Outline each Plasmodium falciparum-infected red blood cell.
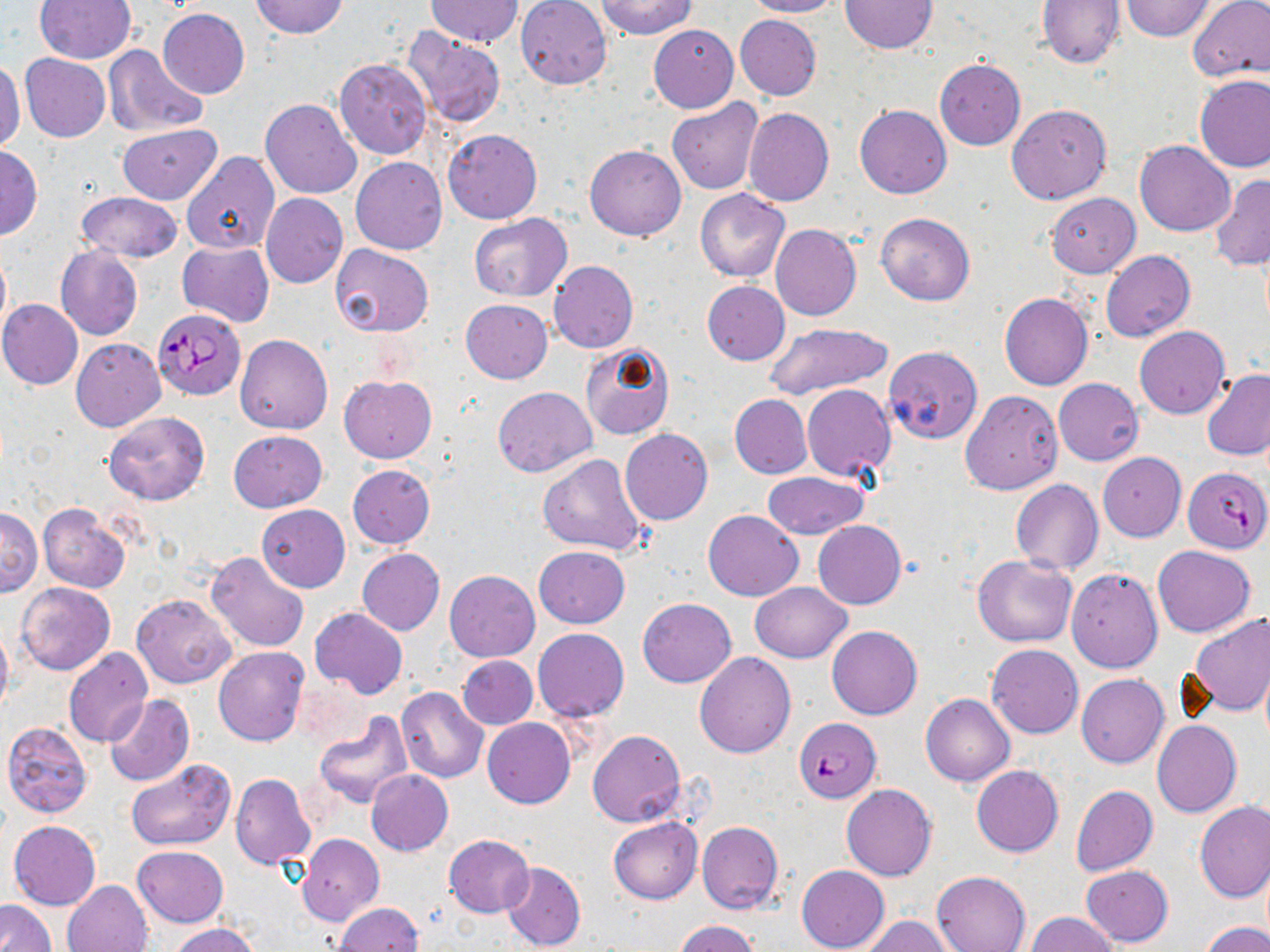

Approximate bounding boxes as named x1/y1/x2/y2 corners in pixels.
Plasmodium falciparum-infected red blood cells: (x1=152, y1=310, x2=245, y2=400), (x1=1184, y1=467, x2=1269, y2=553), (x1=793, y1=717, x2=881, y2=802).

slide-level diagnosis = Plasmodium falciparum
image size = 1270×952 pixels
preparation = thin blood film
modality = optical microscopy
stain = May-Grünwald-Giemsa
uninfected red blood cell locations = approximate bounding boxes as named x1/y1/x2/y2 corners in pixels: (x1=35, y1=0, x2=135, y2=64), (x1=250, y1=0, x2=349, y2=39), (x1=515, y1=0, x2=612, y2=89), (x1=742, y1=0, x2=841, y2=18), (x1=1038, y1=0, x2=1124, y2=68), (x1=1122, y1=0, x2=1214, y2=42), (x1=1186, y1=0, x2=1270, y2=83), (x1=425, y1=1, x2=522, y2=47), (x1=595, y1=1, x2=696, y2=39), (x1=838, y1=1, x2=935, y2=53), (x1=158, y1=8, x2=250, y2=99), (x1=735, y1=15, x2=822, y2=101), (x1=649, y1=25, x2=739, y2=113), (x1=401, y1=28, x2=506, y2=127), (x1=102, y1=45, x2=207, y2=138), (x1=21, y1=54, x2=109, y2=142), (x1=0, y1=59, x2=25, y2=155), (x1=335, y1=59, x2=432, y2=159), (x1=934, y1=59, x2=1026, y2=151), (x1=1194, y1=74, x2=1270, y2=172), (x1=261, y1=98, x2=362, y2=199), (x1=667, y1=98, x2=764, y2=195), (x1=855, y1=104, x2=951, y2=198), (x1=1007, y1=104, x2=1111, y2=204), (x1=743, y1=107, x2=833, y2=206), (x1=116, y1=123, x2=221, y2=204), (x1=443, y1=129, x2=542, y2=224), (x1=1134, y1=140, x2=1235, y2=236), (x1=585, y1=144, x2=686, y2=240), (x1=0, y1=146, x2=43, y2=239), (x1=181, y1=152, x2=279, y2=254), (x1=351, y1=157, x2=447, y2=255), (x1=1211, y1=174, x2=1270, y2=272), (x1=694, y1=189, x2=789, y2=282), (x1=77, y1=191, x2=183, y2=262), (x1=260, y1=193, x2=347, y2=288), (x1=1047, y1=193, x2=1141, y2=278), (x1=875, y1=212, x2=974, y2=305), (x1=469, y1=213, x2=572, y2=301), (x1=770, y1=224, x2=861, y2=322), (x1=178, y1=241, x2=274, y2=327), (x1=329, y1=243, x2=435, y2=338), (x1=55, y1=246, x2=142, y2=340), (x1=0, y1=249, x2=10, y2=341), (x1=1100, y1=250, x2=1195, y2=343), (x1=548, y1=260, x2=638, y2=353), (x1=702, y1=281, x2=790, y2=365), (x1=1000, y1=294, x2=1094, y2=391), (x1=0, y1=300, x2=83, y2=389), (x1=460, y1=300, x2=552, y2=383), (x1=765, y1=321, x2=894, y2=400), (x1=1135, y1=326, x2=1229, y2=418), (x1=235, y1=333, x2=332, y2=434), (x1=71, y1=338, x2=166, y2=432), (x1=580, y1=342, x2=674, y2=441), (x1=882, y1=346, x2=983, y2=443), (x1=1202, y1=370, x2=1270, y2=461), (x1=339, y1=374, x2=436, y2=463), (x1=1053, y1=378, x2=1143, y2=466), (x1=802, y1=384, x2=896, y2=481), (x1=493, y1=387, x2=596, y2=477), (x1=959, y1=389, x2=1063, y2=494), (x1=730, y1=394, x2=812, y2=479), (x1=104, y1=411, x2=210, y2=505), (x1=620, y1=428, x2=714, y2=525), (x1=229, y1=430, x2=327, y2=512), (x1=1097, y1=452, x2=1187, y2=541), (x1=537, y1=453, x2=650, y2=557), (x1=348, y1=464, x2=435, y2=548), (x1=763, y1=471, x2=867, y2=538), (x1=1011, y1=481, x2=1102, y2=575), (x1=38, y1=502, x2=130, y2=593), (x1=256, y1=505, x2=349, y2=592), (x1=0, y1=508, x2=42, y2=596), (x1=703, y1=509, x2=803, y2=601), (x1=813, y1=521, x2=906, y2=609), (x1=1151, y1=545, x2=1255, y2=637), (x1=533, y1=546, x2=629, y2=628), (x1=357, y1=548, x2=444, y2=636), (x1=206, y1=551, x2=310, y2=652), (x1=972, y1=554, x2=1077, y2=646), (x1=1066, y1=569, x2=1162, y2=672), (x1=445, y1=570, x2=539, y2=661), (x1=16, y1=582, x2=115, y2=675), (x1=751, y1=582, x2=852, y2=662), (x1=132, y1=593, x2=237, y2=688), (x1=637, y1=598, x2=736, y2=687), (x1=309, y1=608, x2=408, y2=700), (x1=1186, y1=612, x2=1270, y2=718), (x1=0, y1=621, x2=12, y2=718), (x1=827, y1=625, x2=922, y2=719), (x1=532, y1=627, x2=628, y2=722), (x1=986, y1=645, x2=1083, y2=739), (x1=213, y1=646, x2=309, y2=746), (x1=63, y1=647, x2=152, y2=748), (x1=694, y1=651, x2=797, y2=757), (x1=456, y1=654, x2=538, y2=729), (x1=1077, y1=673, x2=1168, y2=767), (x1=396, y1=687, x2=488, y2=783), (x1=104, y1=694, x2=194, y2=787), (x1=921, y1=694, x2=1014, y2=786), (x1=313, y1=713, x2=413, y2=809), (x1=482, y1=717, x2=576, y2=807), (x1=1152, y1=720, x2=1242, y2=817), (x1=3, y1=722, x2=93, y2=819), (x1=587, y1=730, x2=685, y2=827), (x1=126, y1=757, x2=237, y2=851), (x1=972, y1=765, x2=1063, y2=857), (x1=365, y1=769, x2=453, y2=855), (x1=231, y1=773, x2=316, y2=870), (x1=842, y1=784, x2=936, y2=881), (x1=1071, y1=784, x2=1158, y2=875), (x1=1194, y1=802, x2=1270, y2=903), (x1=609, y1=817, x2=702, y2=904), (x1=8, y1=820, x2=101, y2=910), (x1=697, y1=821, x2=783, y2=914), (x1=297, y1=833, x2=383, y2=926), (x1=443, y1=834, x2=534, y2=918), (x1=132, y1=845, x2=228, y2=926), (x1=501, y1=860, x2=585, y2=952), (x1=796, y1=865, x2=889, y2=951), (x1=1080, y1=865, x2=1173, y2=946), (x1=931, y1=871, x2=1029, y2=952), (x1=62, y1=880, x2=152, y2=952), (x1=0, y1=900, x2=55, y2=952), (x1=334, y1=902, x2=423, y2=952), (x1=1024, y1=912, x2=1119, y2=952), (x1=860, y1=915, x2=956, y2=951), (x1=675, y1=920, x2=757, y2=952), (x1=169, y1=923, x2=262, y2=952), (x1=1201, y1=923, x2=1270, y2=952)
field of view = single
magnification = 1000x